Locate every blood parasite and identify its species.
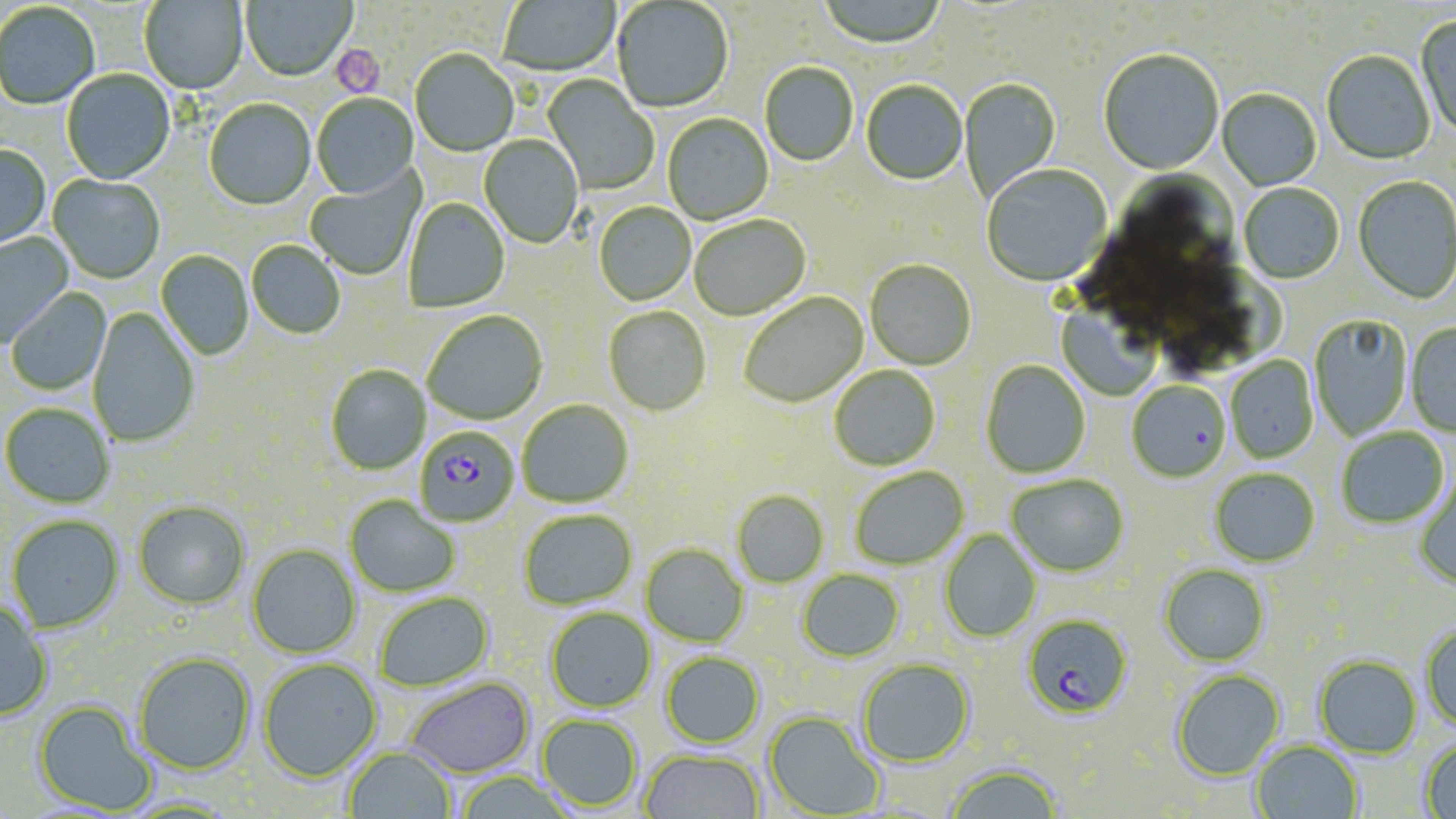
Approximate bounding boxes as (x1,y1)-(x2,y2) corner pairs in pixels.
Plasmodium falciparum-infected red blood cells: (415,426)-(519,527), (1022,614)-(1133,720).
No Plasmodium ovale, Plasmodium malariae, Plasmodium vivax, Babesia divergens, or Trypanosoma brucei observed.

Platelet locations: (331,45)-(385,97). Uninfected red blood cell locations: (240,0)-(356,83), (816,0)-(948,51), (140,1)-(248,95), (498,1)-(620,78), (612,1)-(733,114), (0,4)-(100,111), (1415,14)-(1456,142), (1098,50)-(1224,176), (410,51)-(518,158), (1321,52)-(1435,166), (759,63)-(859,167), (61,70)-(176,186), (542,75)-(658,195), (959,77)-(1061,200), (861,82)-(967,187), (1217,89)-(1322,191), (312,94)-(418,200), (204,100)-(316,211), (662,114)-(774,226), (478,135)-(583,249), (0,146)-(51,252), (981,166)-(1112,289), (305,171)-(423,280), (1115,172)-(1235,261), (47,175)-(165,284), (1352,176)-(1456,306), (1239,184)-(1344,286), (404,198)-(510,312), (594,203)-(695,306), (689,216)-(811,322), (0,231)-(74,346), (246,241)-(345,339), (155,250)-(254,360), (865,260)-(977,371), (6,288)-(112,397), (738,292)-(869,410), (1056,292)-(1162,400), (603,306)-(711,417), (87,308)-(200,448), (422,310)-(548,425), (1310,315)-(1414,440), (1406,323)-(1456,437), (1225,356)-(1318,464), (980,360)-(1091,478), (325,365)-(431,475), (829,366)-(940,471), (1126,381)-(1230,483), (517,399)-(633,508), (1,403)-(115,508), (1336,428)-(1449,529), (849,467)-(969,570), (1209,468)-(1319,567), (1006,475)-(1128,577), (1414,478)-(1456,590), (731,491)-(829,587), (345,495)-(460,597), (133,500)-(250,609), (518,510)-(637,610), (6,515)-(124,633), (939,530)-(1042,642), (247,544)-(361,658), (641,544)-(748,647), (1159,564)-(1269,666), (797,570)-(904,662), (373,591)-(494,692), (0,602)-(53,721), (545,607)-(656,712), (1421,624)-(1456,733), (660,650)-(765,748), (133,652)-(256,775), (1313,654)-(1422,758), (257,658)-(382,782), (857,658)-(975,767), (1171,668)-(1285,780), (403,676)-(535,778), (33,700)-(156,815), (763,711)-(885,817), (537,714)-(643,812), (1419,737)-(1456,819), (1252,741)-(1363,819), (344,746)-(456,819), (639,749)-(764,819), (943,763)-(1065,819), (452,772)-(577,819). Slide-level diagnosis: Plasmodium falciparum. Thin blood smear. Image is 1456×819 pixels. 1000x magnification. One field of a larger specimen. May-Grünwald-Giemsa stain. Light microscopy.